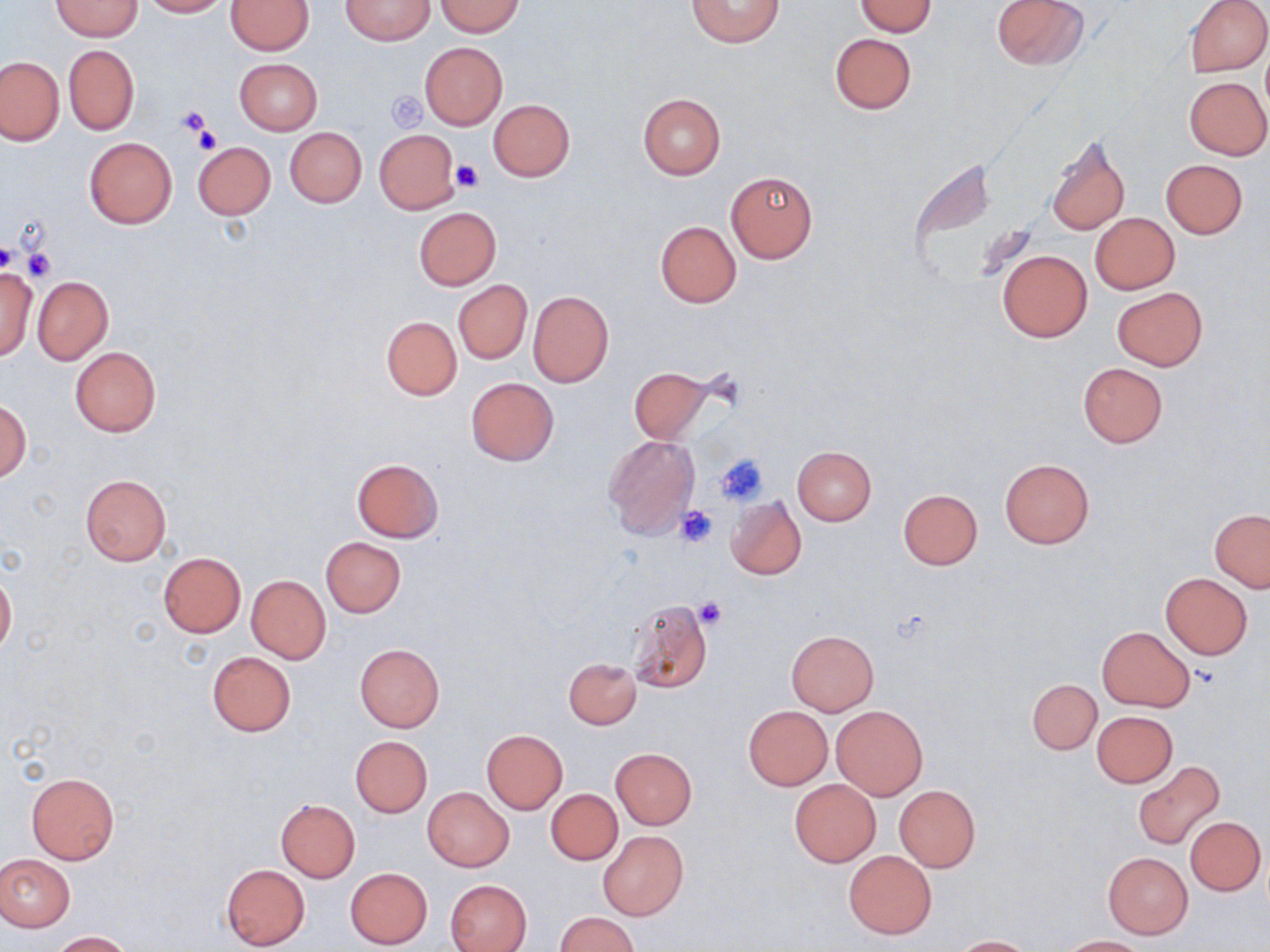
slide-level diagnosis = negative for blood parasites
modality = light microscopy
stain = May-Grünwald-Giemsa
platelet locations = approximate bounding boxes as (x1, y1, x2, y2) in pixels: (385, 92, 427, 132), (176, 107, 212, 140), (192, 127, 222, 156), (453, 161, 485, 193), (0, 241, 16, 274), (22, 247, 57, 282), (714, 452, 768, 507), (674, 506, 718, 549), (693, 597, 727, 630)
uninfected red blood cell locations = approximate bounding boxes as (x1, y1, x2, y2) in pixels: (139, 0, 228, 17), (341, 0, 434, 45), (687, 0, 785, 47), (990, 0, 1089, 71), (1184, 0, 1270, 76), (52, 1, 142, 40), (226, 1, 314, 55), (435, 1, 524, 36), (854, 2, 937, 36), (829, 33, 917, 113), (420, 43, 507, 129), (64, 45, 138, 135), (0, 55, 65, 145), (235, 58, 322, 134), (1184, 76, 1270, 159), (638, 93, 725, 180), (488, 99, 574, 181), (284, 126, 367, 207), (374, 130, 460, 212), (1045, 134, 1129, 236), (84, 137, 176, 229), (193, 141, 276, 220), (1161, 160, 1248, 239), (726, 171, 818, 262), (413, 207, 500, 290), (1089, 212, 1180, 294), (654, 221, 742, 309), (996, 249, 1092, 342), (0, 266, 36, 360), (33, 277, 112, 363), (453, 280, 531, 363), (1112, 287, 1207, 371), (527, 290, 614, 387), (381, 315, 462, 400), (70, 346, 161, 437), (1077, 363, 1168, 448), (627, 367, 723, 446), (465, 377, 560, 465), (0, 399, 32, 482), (604, 434, 700, 538), (792, 445, 877, 525), (351, 458, 445, 542), (999, 459, 1095, 548), (80, 474, 171, 564), (898, 488, 983, 570), (726, 496, 806, 581), (1209, 509, 1269, 592), (321, 537, 406, 617), (158, 552, 246, 637), (0, 571, 16, 657), (1161, 573, 1253, 658), (247, 575, 330, 663), (626, 599, 713, 694), (1097, 626, 1195, 711), (786, 630, 878, 715), (355, 643, 444, 731), (207, 651, 297, 737), (563, 657, 642, 728), (1027, 678, 1101, 755), (831, 705, 928, 799), (743, 706, 832, 789), (1091, 711, 1177, 787), (481, 730, 568, 814), (350, 736, 433, 817), (611, 748, 697, 829), (1132, 760, 1225, 851), (25, 772, 120, 865), (790, 779, 880, 866), (894, 785, 980, 872), (422, 787, 514, 872), (546, 789, 621, 865), (275, 799, 360, 881), (1186, 816, 1266, 895), (597, 831, 688, 921), (843, 850, 937, 938), (1102, 850, 1193, 939), (0, 854, 75, 931), (221, 864, 311, 950), (344, 867, 433, 949), (445, 879, 531, 952), (555, 912, 640, 952), (47, 930, 134, 951), (952, 935, 1035, 951), (1056, 935, 1152, 951)
preparation = thin blood smear
image size = 1270×952 pixels
magnification = 1000x
field of view = one of a larger specimen